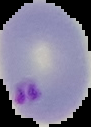 From a thin blood smear. Result: malaria parasites detected. Image is 91×127 pixels. The area outside the segmented cell region is set to black.